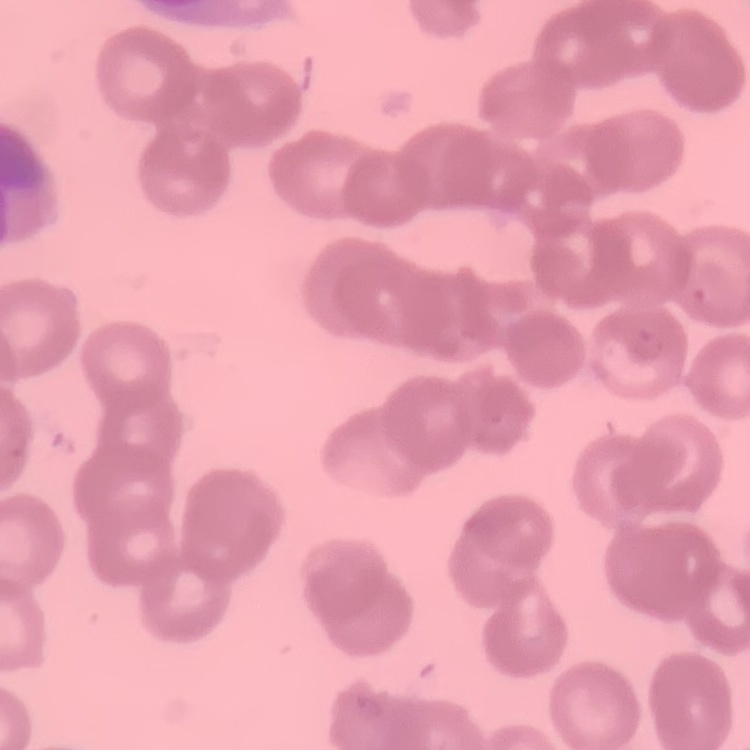
The erythrocytes show rouleaux formation. One tile cut from a larger photomicrograph. Thin peripheral smear. Stained with either Field's or Giemsa.